Report the malaria status of this cell.
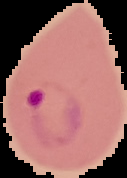
It is parasitized.

image type = segmented cell region with the area outside set to black
preparation = thin blood film
image size = 127×178 pixels